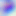
Micrograph. 400x magnification. Toxoplasma gondii is seen.